Report the malaria status of this cell.
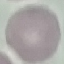
Uninfected.

Summary:
  - Image type: automatically extracted cell patch, resized to 64 × 64 pixels
  - Stain: Giemsa
  - Preparation: thin blood film
  - Capture: smartphone camera at the microscope eyepiece